Assess this cell for malaria.
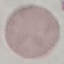
Uninfected.

Summary:
  - Capture: smartphone camera at the microscope eyepiece
  - Stain: Giemsa
  - Preparation: thin smear
  - Image type: automatically extracted cell patch, resized to 64 × 64 pixels